Classify this cell by malaria status.
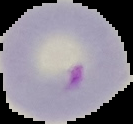

Parasitized.

{
  "preparation": "thin blood smear",
  "image_size": "133×124 pixels",
  "image_type": "segmented cell region on a black background"
}